Identify the preparation type.
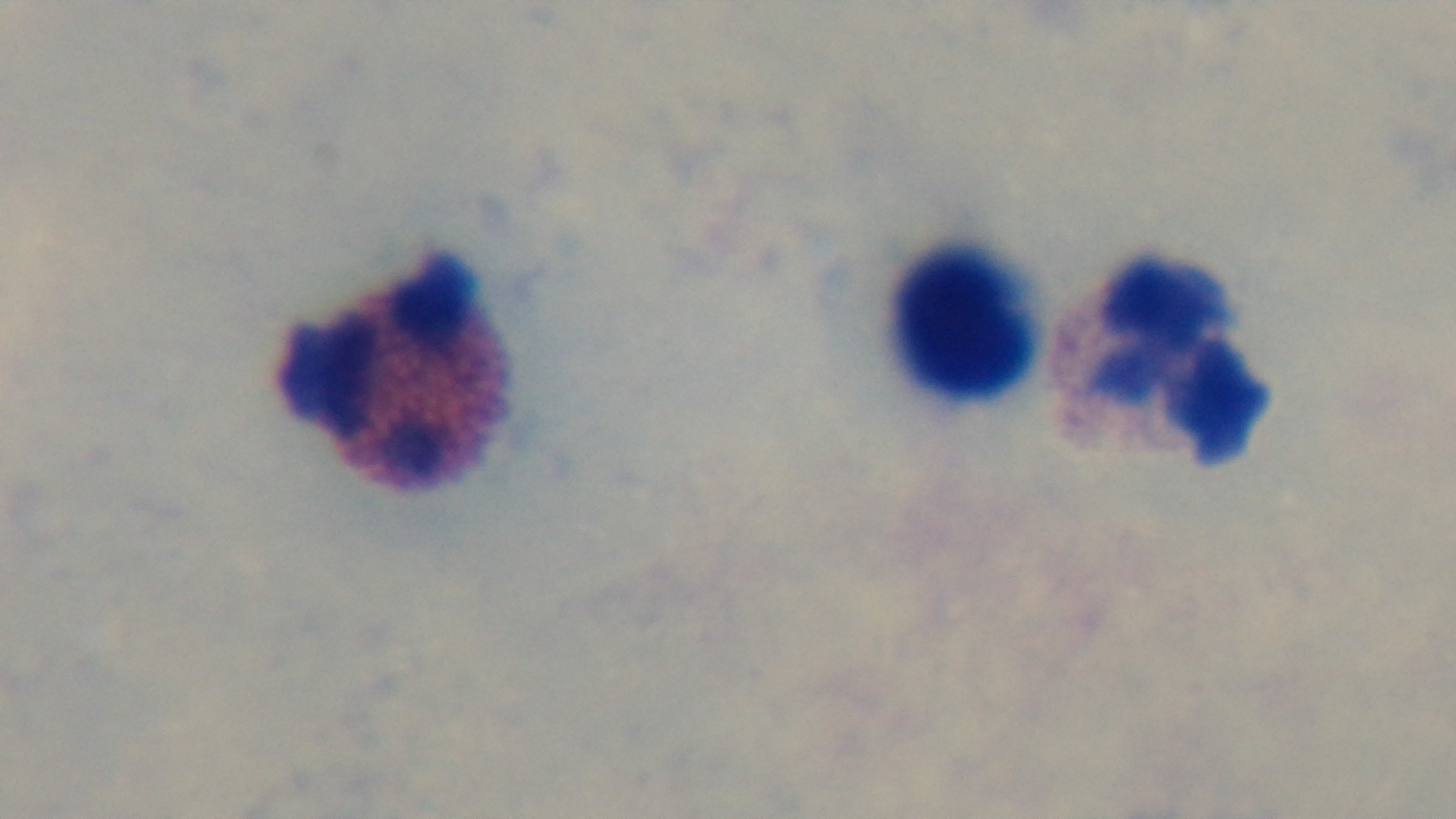

Thick.

malaria_status: uninfected
stain: Giemsa
field_of_view: one from the slide
modality: light microscopy
objective: 100x oil immersion
capture: mounted 4K digital camera